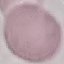
Malaria status: uninfected. Giemsa-stained preparation. Cell patch, automatically extracted from a larger field of view and resized to 64 × 64 pixels. Acquired by smartphone through the microscope eyepiece. Thin blood film.